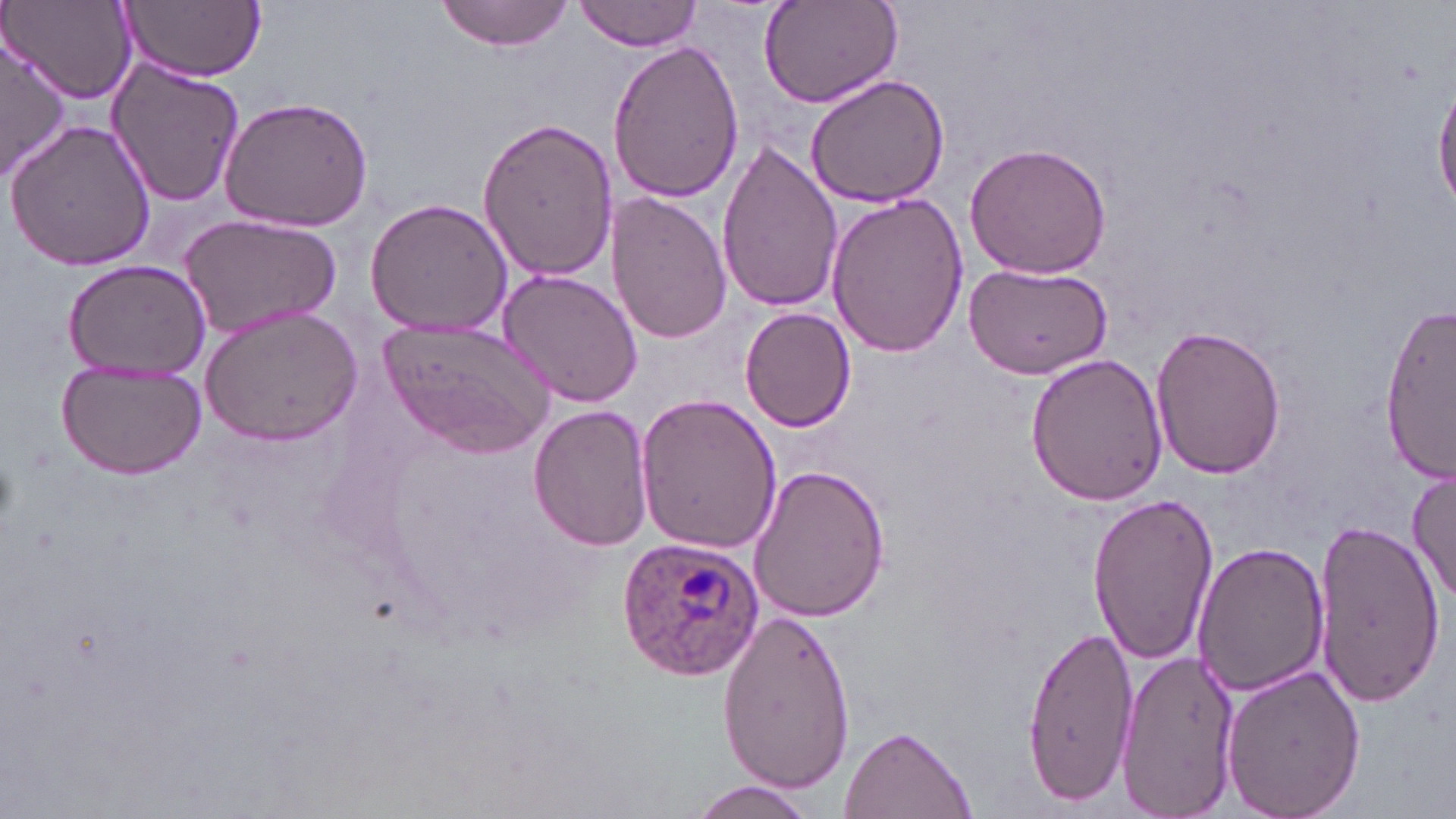 Approximate bounding boxes as (x1, y1, x2, y2) in pixels. Plasmodium ovale-infected red blood cell locations: (615, 538, 768, 683). Uninfected red blood cell locations: (5, 0, 138, 104), (119, 0, 267, 81), (434, 0, 576, 50), (756, 0, 902, 110), (575, 1, 701, 52), (3, 33, 73, 177), (608, 39, 745, 207), (103, 55, 246, 207), (804, 73, 951, 209), (1433, 77, 1456, 217), (218, 95, 375, 233), (476, 117, 618, 281), (5, 118, 157, 273), (715, 140, 844, 314), (964, 142, 1112, 280), (825, 191, 970, 356), (607, 194, 730, 345), (363, 197, 515, 339), (179, 213, 342, 339), (62, 260, 211, 383), (963, 262, 1113, 381), (497, 269, 643, 408), (1380, 301, 1455, 482), (199, 305, 363, 445), (739, 307, 857, 433), (382, 319, 552, 456), (1149, 325, 1287, 481), (1026, 354, 1169, 506), (54, 359, 207, 478), (633, 392, 783, 556), (528, 405, 654, 549), (744, 465, 888, 624), (1407, 466, 1456, 606), (1086, 491, 1219, 664), (1313, 515, 1444, 711), (1195, 542, 1329, 696), (717, 608, 858, 795), (1023, 623, 1138, 802), (1114, 649, 1238, 816), (1218, 662, 1366, 819), (840, 726, 975, 817), (685, 782, 820, 818). Slide-level diagnosis: Plasmodium ovale. Thin blood film. One field of a larger specimen. Captured at 1000x magnification. Light microscopy. May-Grünwald-Giemsa stain. Image is 1456×819 pixels.